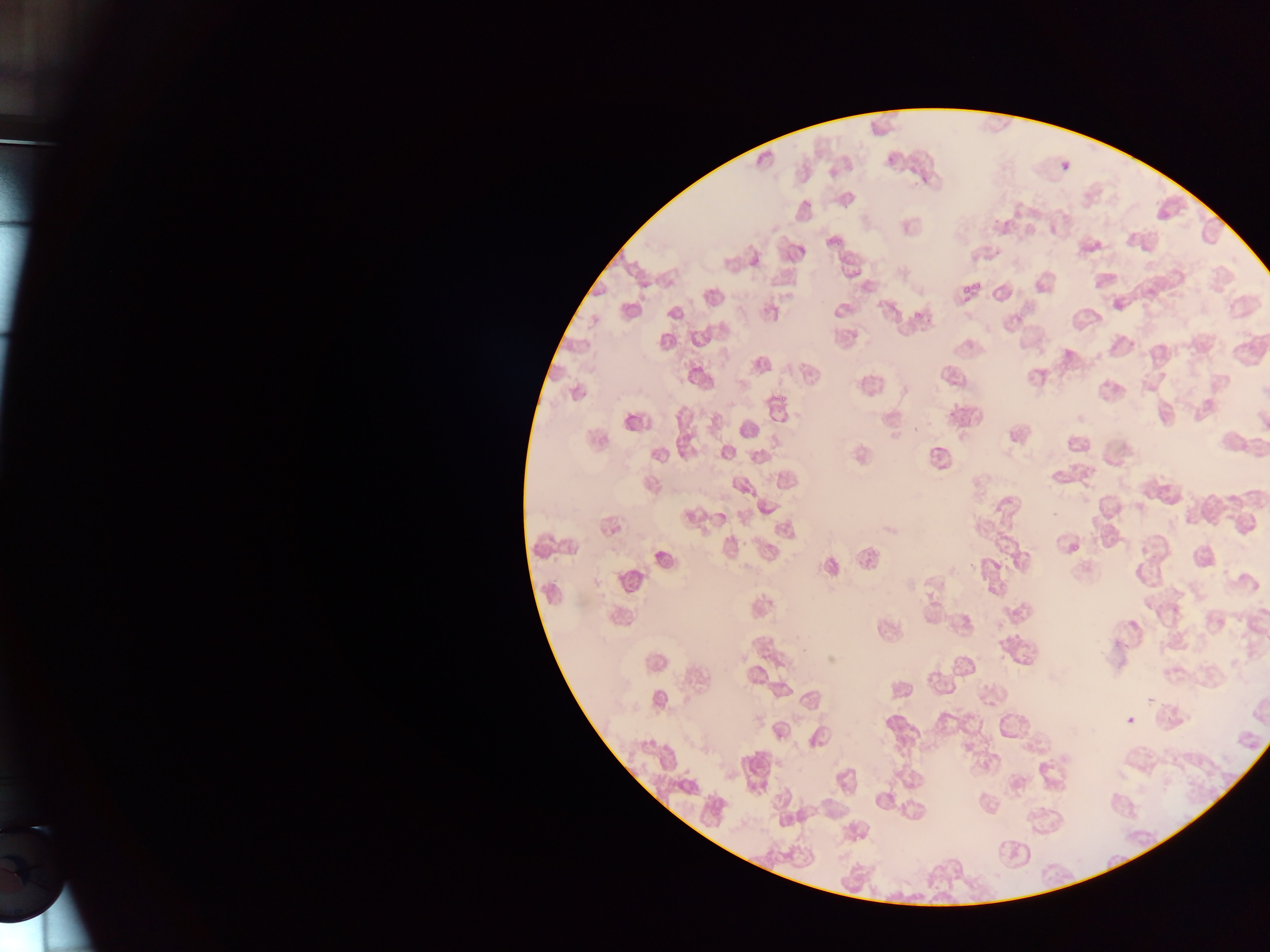 Approximate bounding boxes as {left, top, right, bottom} in pixels. Malaria parasite locations: {887, 155, 897, 164}, {972, 278, 982, 293}, {962, 285, 969, 293}, {960, 296, 974, 304}, {909, 311, 924, 323}. Sample from Ghana. Mobile-phone photograph taken through the microscope. Single field of view. Image is 1270×952 pixels. Thin blood smear.